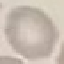
result = negative for malaria parasites
stain = Giemsa
preparation = thin blood film
image type = cell patch, automatically extracted from a larger field of view and resized to 64 × 64 pixels
capture = smartphone through the microscope eyepiece